Identify the cell.
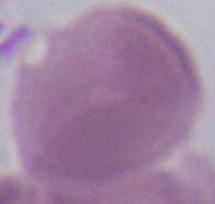

This is an erythrocyte.

Photomicrograph. 1000x magnification.